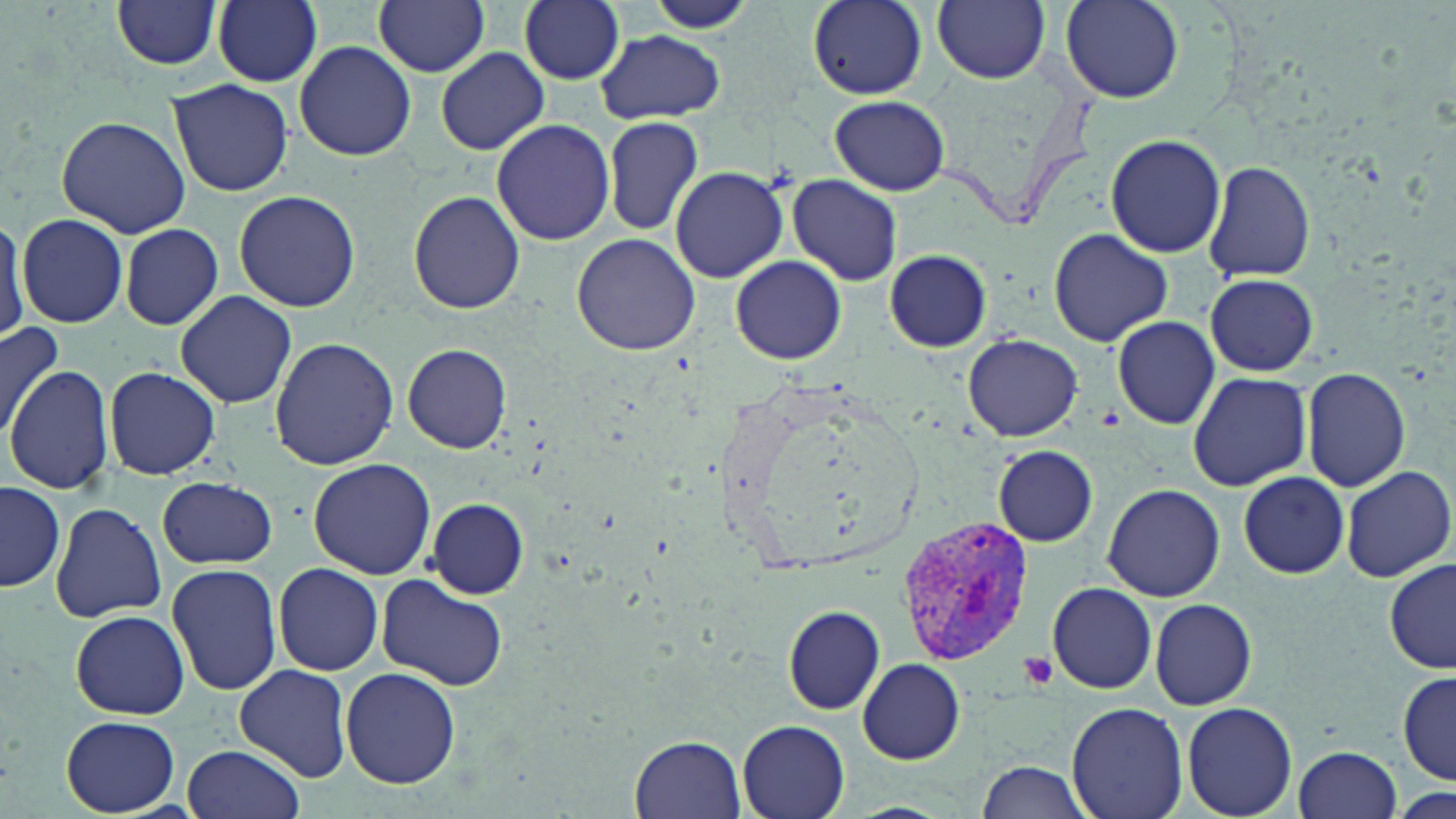
Summary:
  - Coordinate format: approximate bounding boxes as (x1, y1, x2, y2) in pixels
  - Uninfected red blood cell locations: (212, 0, 323, 87), (373, 0, 491, 76), (519, 0, 626, 84), (932, 0, 1049, 85), (112, 1, 220, 71), (642, 1, 762, 33), (1060, 1, 1184, 104), (807, 3, 926, 101), (595, 29, 727, 123), (294, 41, 413, 162), (436, 48, 549, 155), (167, 79, 293, 197), (829, 95, 950, 195), (56, 114, 189, 238), (603, 116, 704, 236), (490, 119, 616, 246), (1104, 134, 1227, 258), (1203, 160, 1316, 283), (669, 167, 789, 282), (786, 176, 903, 287), (233, 191, 362, 313), (409, 191, 524, 315), (0, 214, 28, 343), (17, 214, 129, 327), (118, 223, 223, 330), (1048, 227, 1173, 348), (572, 233, 700, 355), (883, 250, 993, 352), (731, 255, 846, 365), (1205, 273, 1318, 376), (175, 290, 297, 408), (1110, 318, 1224, 428), (0, 319, 66, 441), (962, 333, 1083, 442), (268, 337, 399, 471), (403, 344, 512, 454), (104, 364, 221, 480), (1300, 366, 1412, 493), (4, 367, 115, 495), (1187, 372, 1312, 492), (994, 445, 1098, 547), (308, 459, 437, 579), (1338, 464, 1455, 582), (1238, 472, 1349, 578), (158, 478, 278, 568), (1, 482, 65, 592), (1103, 482, 1226, 603), (425, 497, 530, 599), (49, 502, 167, 622), (1385, 559, 1455, 675), (165, 562, 283, 694), (272, 563, 385, 677), (375, 577, 510, 691), (259, 579, 370, 750), (1046, 582, 1157, 694), (1150, 598, 1257, 711), (784, 605, 884, 714), (71, 610, 189, 719), (856, 658, 965, 765), (235, 664, 353, 783), (340, 667, 461, 789), (1396, 671, 1455, 785), (1067, 701, 1189, 819), (1183, 702, 1298, 818), (60, 715, 181, 816), (737, 720, 849, 819), (632, 734, 747, 819), (183, 744, 307, 819), (1291, 745, 1402, 819), (974, 760, 1094, 819)
  - Plasmodium vivax-infected red blood cell locations: (895, 514, 1039, 665)
  - Platelet locations: (1019, 651, 1060, 691)
  - Slide-level diagnosis: Plasmodium vivax
  - Stain: May-Grünwald-Giemsa
  - Modality: optical microscopy
  - Magnification: 1000x
  - Preparation: thin blood film
  - Field of view: single
  - Image size: 1456×819 pixels